Outline each Plasmodium vivax-infected red blood cell.
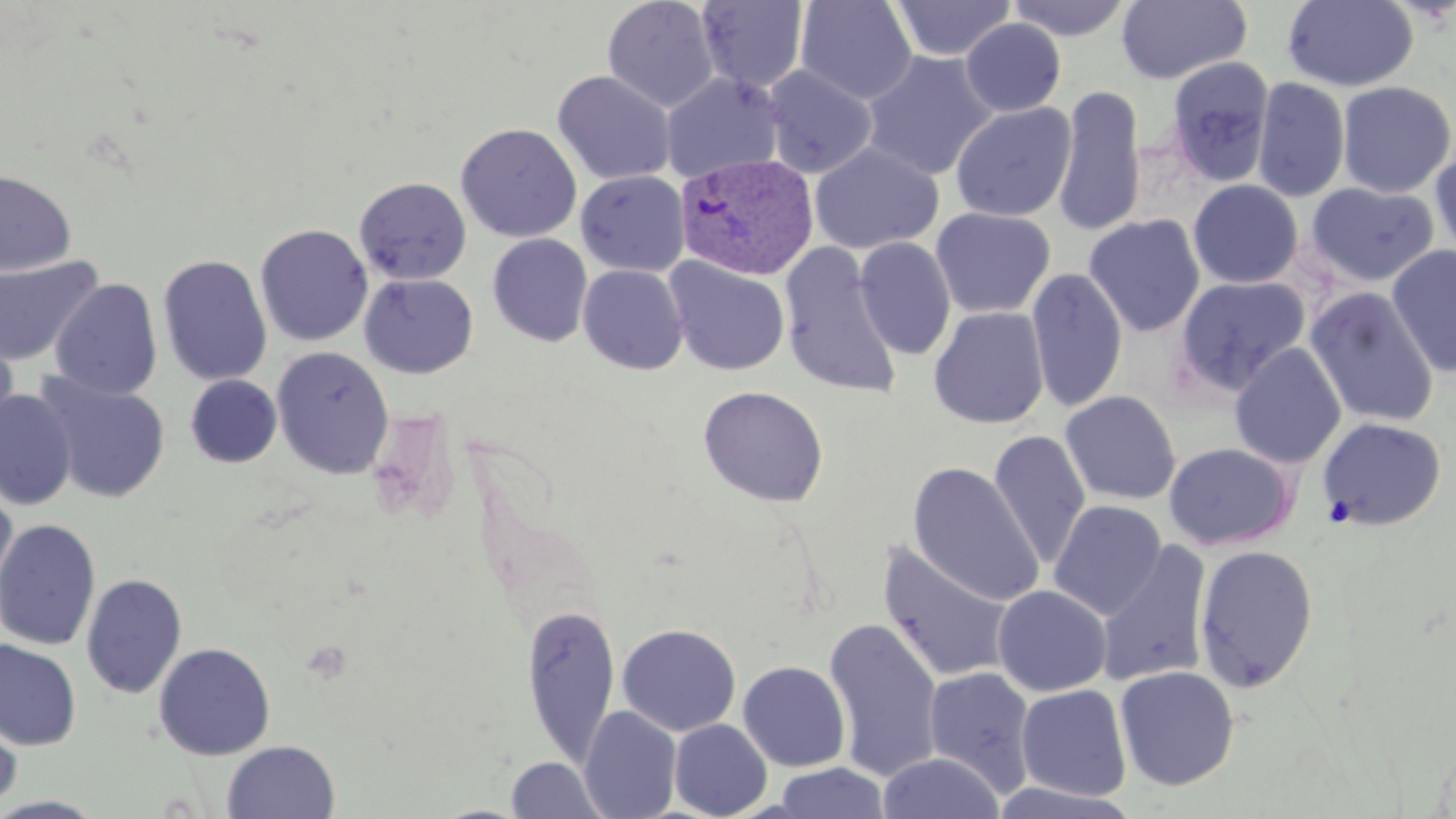

Approximate bounding boxes as (x1, y1, x2, y2) in pixels.
Plasmodium vivax-infected red blood cells: (675, 152, 818, 281).

Summary:
  - Uninfected red blood cell locations: (602, 0, 720, 112), (795, 0, 918, 104), (890, 0, 1017, 61), (1005, 0, 1133, 41), (1116, 0, 1252, 85), (1282, 0, 1418, 92), (696, 1, 809, 92), (960, 18, 1066, 117), (861, 50, 998, 181), (1165, 56, 1276, 187), (762, 64, 878, 178), (552, 71, 676, 185), (660, 71, 783, 182), (1252, 77, 1349, 202), (1336, 80, 1456, 198), (1054, 85, 1146, 237), (950, 102, 1077, 222), (455, 123, 582, 243), (1430, 141, 1456, 261), (809, 143, 942, 254), (0, 170, 76, 276), (575, 170, 690, 276), (354, 176, 472, 285), (1188, 180, 1303, 289), (1305, 182, 1439, 287), (930, 207, 1055, 319), (1082, 214, 1206, 338), (255, 224, 373, 346), (487, 234, 593, 347), (854, 236, 956, 359), (778, 243, 900, 398), (1387, 245, 1456, 378), (0, 254, 103, 367), (157, 254, 273, 386), (664, 256, 791, 376), (578, 264, 689, 374), (1026, 267, 1128, 412), (359, 273, 478, 379), (1174, 275, 1309, 397), (49, 278, 163, 400), (1304, 286, 1439, 428), (928, 306, 1049, 428), (0, 336, 20, 459), (1229, 343, 1346, 468), (271, 346, 394, 480), (34, 371, 172, 504), (184, 374, 282, 468), (697, 385, 829, 508), (0, 390, 78, 509), (1060, 391, 1181, 505), (1317, 416, 1447, 531), (988, 430, 1092, 568), (1164, 442, 1295, 550), (907, 461, 1045, 606), (0, 480, 18, 612), (1049, 499, 1167, 620), (0, 519, 102, 651), (1095, 541, 1213, 687), (877, 542, 1018, 684), (1194, 544, 1319, 693), (81, 573, 187, 699), (992, 585, 1112, 697), (520, 603, 620, 769), (823, 619, 944, 783), (616, 624, 741, 736), (0, 638, 82, 750), (153, 642, 276, 760), (738, 661, 851, 772), (1114, 665, 1240, 791), (923, 666, 1037, 795), (1016, 684, 1132, 801), (0, 694, 23, 814), (579, 706, 682, 819), (669, 718, 772, 818), (222, 740, 340, 818), (877, 752, 1005, 819), (505, 756, 610, 818), (773, 762, 892, 819), (990, 781, 1139, 817), (0, 794, 109, 818)
  - Slide-level diagnosis: Plasmodium vivax
  - Magnification: 1000x
  - Stain: May-Grünwald-Giemsa
  - Preparation: thin blood film
  - Modality: optical microscopy
  - Field of view: single
  - Image size: 1456×819 pixels